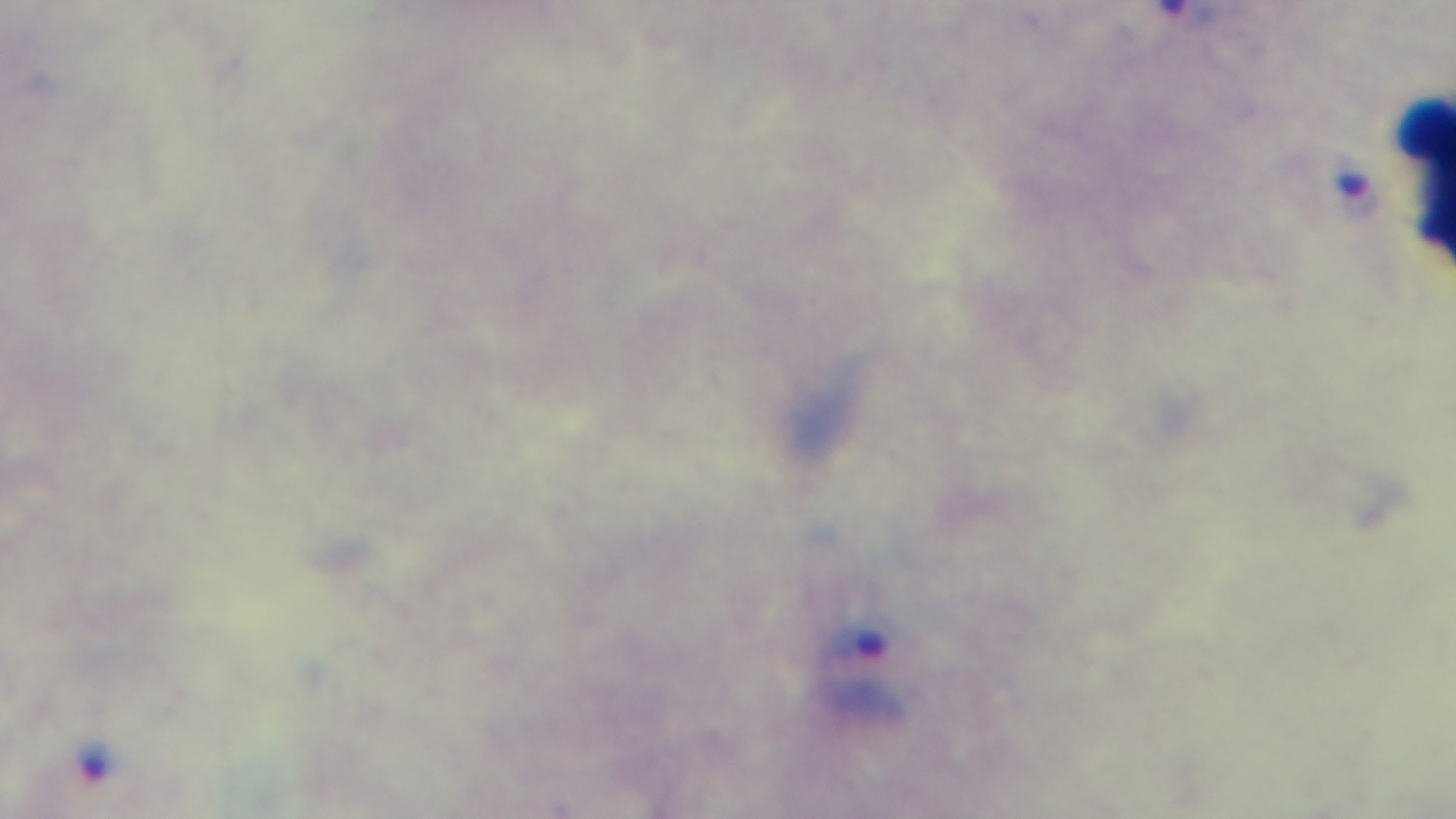

Summary:
  - Capture: mounted 4K digital camera
  - Field of view: single
  - Stain: Giemsa
  - Objective: 100x oil immersion
  - Preparation: thick
  - Modality: light microscopy
  - Malaria status: positive